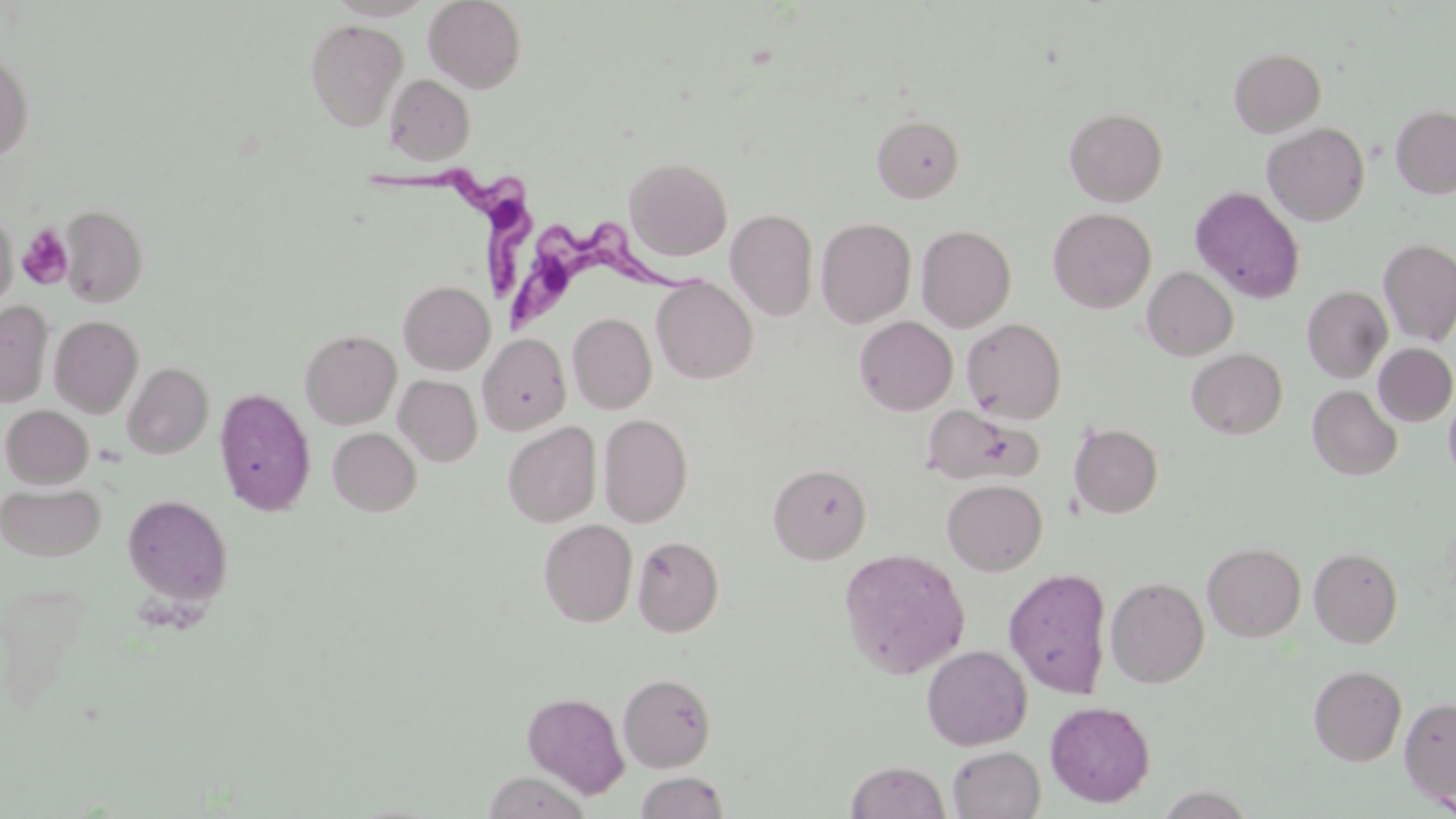

Approximate bounding boxes as (x1,y1)-(x2,y2) corner pairs in pixels. Trypanosoma brucei locations: (371,161)-(539,305), (503,219)-(705,341). Platelet locations: (17,223)-(73,288). Uninfected red blood cell locations: (423,0)-(527,93), (305,19)-(407,131), (1229,47)-(1327,137), (0,48)-(34,162), (384,74)-(475,166), (1391,105)-(1456,198), (1064,107)-(1168,207), (872,114)-(964,202), (1263,122)-(1369,226), (624,156)-(732,261), (1191,186)-(1305,304), (58,203)-(149,308), (1,207)-(17,312), (726,208)-(818,321), (1047,208)-(1156,313), (815,217)-(916,328), (916,224)-(1016,332), (1379,238)-(1456,346), (1142,266)-(1238,361), (651,276)-(758,384), (398,280)-(495,375), (1302,286)-(1392,383), (0,301)-(53,407), (567,313)-(657,414), (50,315)-(143,417), (854,315)-(958,415), (962,317)-(1067,423), (300,329)-(402,429), (478,333)-(570,435), (1374,343)-(1456,427), (1186,348)-(1288,438), (123,362)-(213,460), (394,375)-(482,466), (1308,385)-(1402,481), (1443,386)-(1456,487), (215,387)-(316,516), (921,404)-(1042,486), (1,405)-(94,488), (599,413)-(693,527), (503,421)-(601,527), (1069,423)-(1163,518), (328,428)-(421,515), (768,463)-(871,564), (942,479)-(1047,575), (1,483)-(106,561), (122,494)-(233,606), (539,519)-(637,627), (632,535)-(724,637), (1202,542)-(1306,642), (1309,546)-(1403,648), (838,548)-(971,679), (1004,567)-(1113,698), (1106,576)-(1209,688), (921,645)-(1032,750), (1309,664)-(1407,766), (618,672)-(717,772), (522,691)-(629,798), (1400,697)-(1456,805), (1045,701)-(1155,807), (947,745)-(1045,819), (846,761)-(950,819), (483,771)-(589,818), (635,771)-(730,818). Slide-level diagnosis: Trypanosoma brucei. One field of a larger specimen. 1000x magnification. Image is 1456×819 pixels. Thin blood film. May-Grünwald-Giemsa stain. Light microscopy.